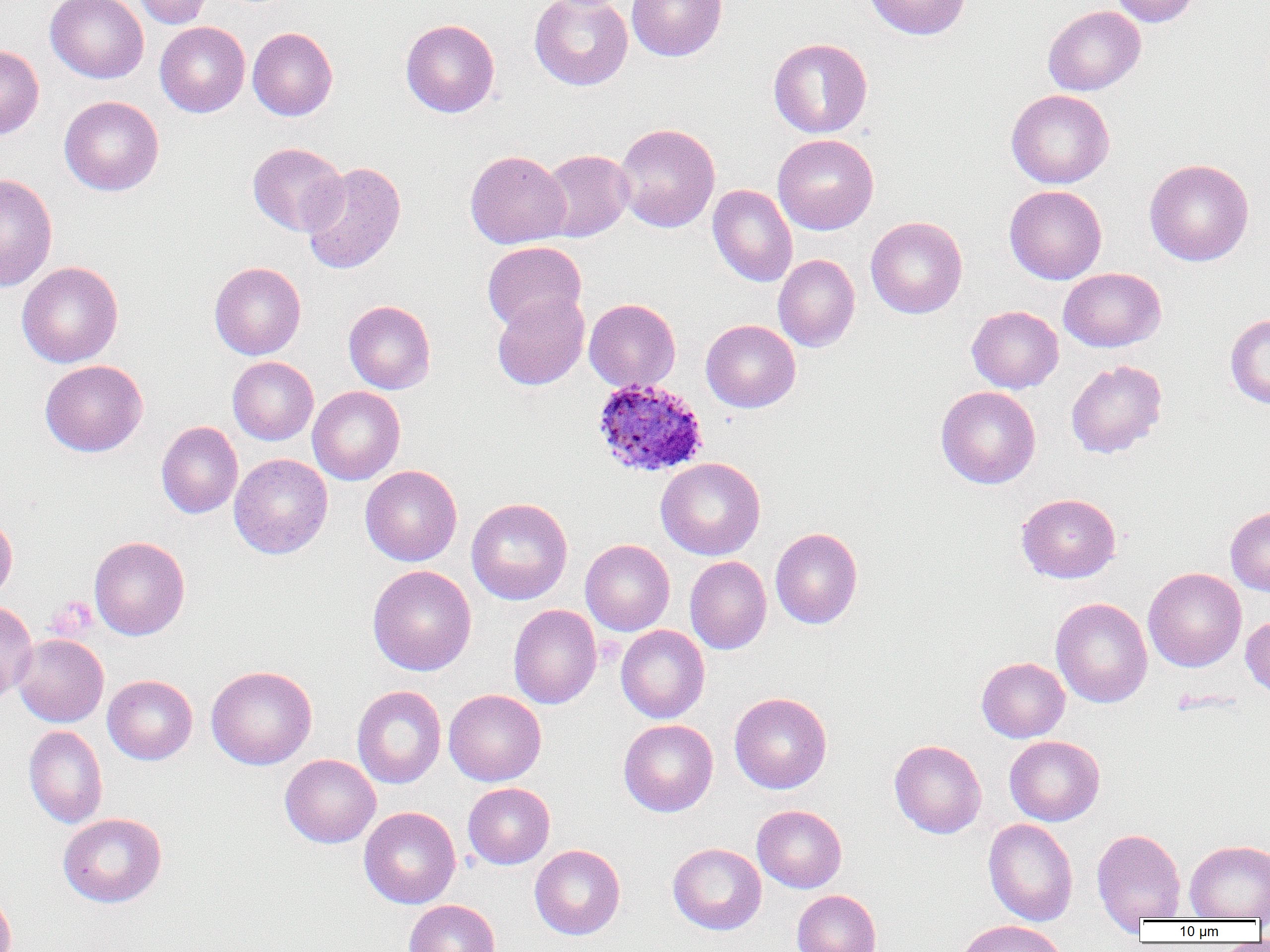
slide_level_diagnosis: Plasmodium ovale
uninfected_red_blood_cell_locations: 'approximate bounding boxes as (x1,y1)-(x2,y2) corner pairs in pixels: (45,0)-(149,83), (133,0)-(213,28), (529,0)-(632,90), (627,0)-(727,61), (864,0)-(970,40), (1109,0)-(1201,27), (1043,5)-(1145,95), (400,19)-(500,117), (155,21)-(250,117), (248,26)-(337,120), (768,37)-(873,138), (0,45)-(44,139), (1006,89)-(1115,188), (59,96)-(164,196), (614,123)-(720,233), (773,133)-(879,235), (247,142)-(348,236), (538,149)-(634,242), (465,150)-(571,249), (1144,158)-(1254,266), (300,162)-(406,275), (0,173)-(58,291), (708,185)-(798,287), (1004,185)-(1107,284), (866,216)-(968,318), (482,241)-(586,332), (773,254)-(860,351), (17,261)-(124,368), (209,262)-(306,359), (1059,268)-(1165,352), (491,293)-(589,390), (584,298)-(680,392), (343,300)-(436,394), (967,305)-(1063,393), (1225,313)-(1270,409), (701,319)-(800,412), (228,356)-(318,445), (40,360)-(147,457), (1066,360)-(1167,458), (307,386)-(405,485), (935,386)-(1041,489), (156,421)-(243,518), (229,453)-(333,559), (655,457)-(765,560), (360,464)-(462,566), (1016,493)-(1121,583), (466,497)-(573,605), (1225,507)-(1270,596), (0,516)-(17,604), (770,527)-(863,629), (89,535)-(190,640), (580,539)-(675,636), (685,556)-(772,654), (367,565)-(476,675), (1143,567)-(1246,672), (1051,597)-(1152,708), (0,601)-(38,701), (509,604)-(601,709), (1241,614)-(1270,699), (616,624)-(709,723), (12,633)-(109,727), (977,657)-(1070,742), (206,665)-(317,769), (103,675)-(198,764), (352,685)-(446,789), (444,689)-(546,786), (729,692)-(832,794), (618,719)-(718,817), (24,725)-(108,828), (1004,735)-(1104,826), (889,739)-(986,838), (280,754)-(381,848), (462,782)-(555,869), (752,804)-(847,893), (359,806)-(461,908), (58,813)-(167,908), (983,818)-(1079,926), (1092,829)-(1186,923), (1185,839)-(1270,920), (668,842)-(766,935), (529,844)-(626,940), (0,886)-(16,952), (792,890)-(881,952), (403,899)-(500,952), (954,919)-(1071,952)'
preparation: thin blood film
modality: light microscopy
field_of_view: one of a larger specimen
image_size: 1270×952 pixels
platelet_locations: 'approximate bounding boxes as (x1,y1)-(x2,y2) corner pairs in pixels: (46,597)-(97,640)'
magnification: 1000x
plasmodium_ovale_infected_red_blood_cell_locations: 'approximate bounding boxes as (x1,y1)-(x2,y2) corner pairs in pixels: (591,377)-(709,478)'